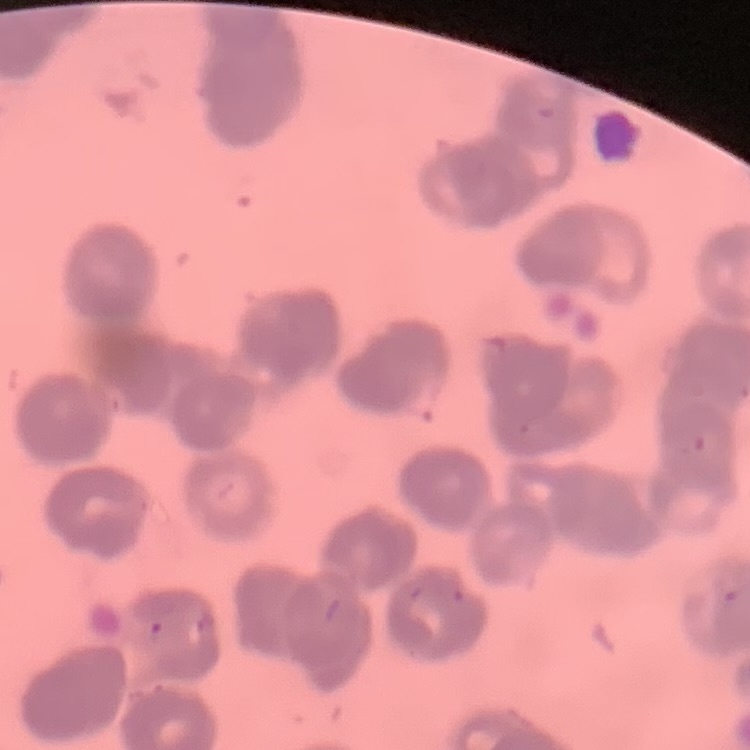
Summary:
  - Red blood cell morphology: rouleaux formation
  - Preparation: thin blood smear
  - Stain: Field's or Giemsa
  - Image type: square crop of a larger photomicrograph